Locate every leukocyte (white blood cell).
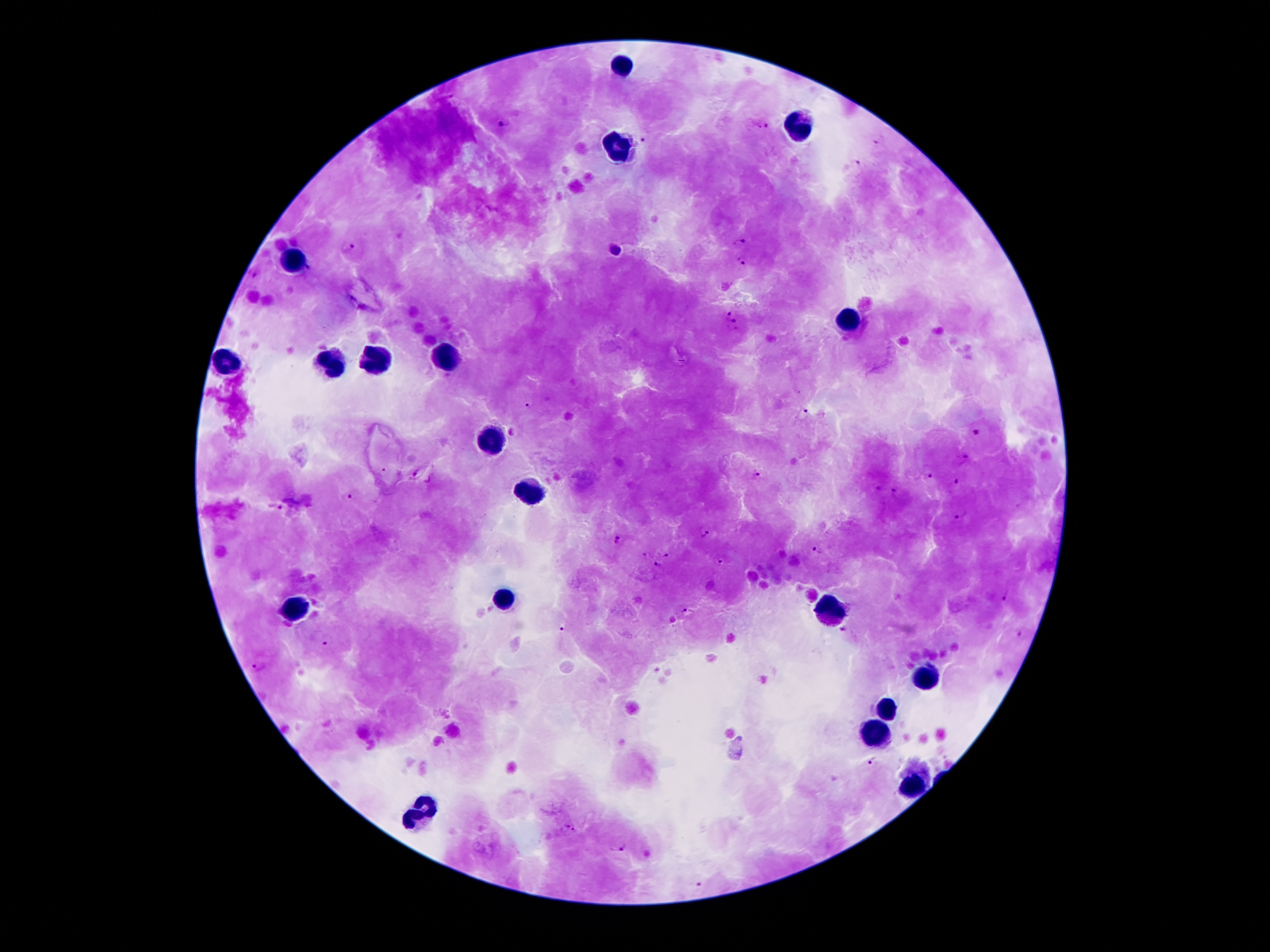
Approximate centers as [x, y] in pixels.
Leukocytes: [625, 62], [796, 118], [622, 148], [294, 258], [852, 319], [370, 361], [230, 362], [443, 362], [333, 365], [490, 443], [527, 493], [507, 596], [826, 606], [291, 608], [924, 676], [885, 709], [874, 734], [910, 785], [417, 813].

Plasmodium parasite locations: [503, 122], [761, 126], [645, 138], [877, 141], [857, 164], [738, 242], [348, 247], [617, 251], [740, 261], [255, 273], [726, 312], [736, 326], [530, 406], [804, 413], [975, 433], [961, 458], [926, 473], [758, 476], [956, 484], [877, 489], [895, 492], [347, 499], [275, 508], [960, 513], [704, 534], [617, 540], [818, 551], [666, 554], [719, 563], [656, 566], [1008, 595], [689, 612], [563, 627], [844, 630], [1021, 634], [327, 641], [258, 666], [873, 760], [569, 829], [620, 847], [701, 885]. Patient malaria status: positive for Plasmodium falciparum. Photographed through the microscope eyepiece with a smartphone camera. 100x magnification. One field from this slide. Image is 1270×952 pixels. Thick blood smear. Giemsa-stained preparation.